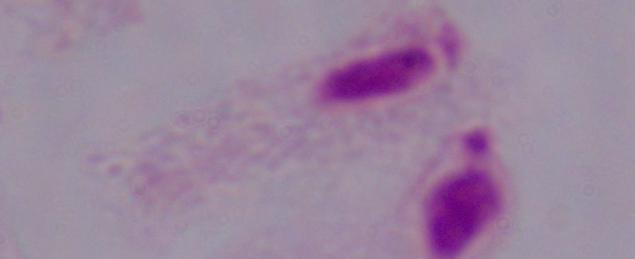

A trichomonad is shown. Photomicrograph. 1000x magnification.